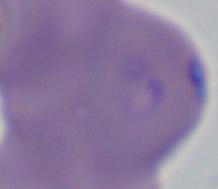
Summary:
  - Identification: Babesia
  - Magnification: 1000x
  - Modality: micrograph